Point out each leukocyte.
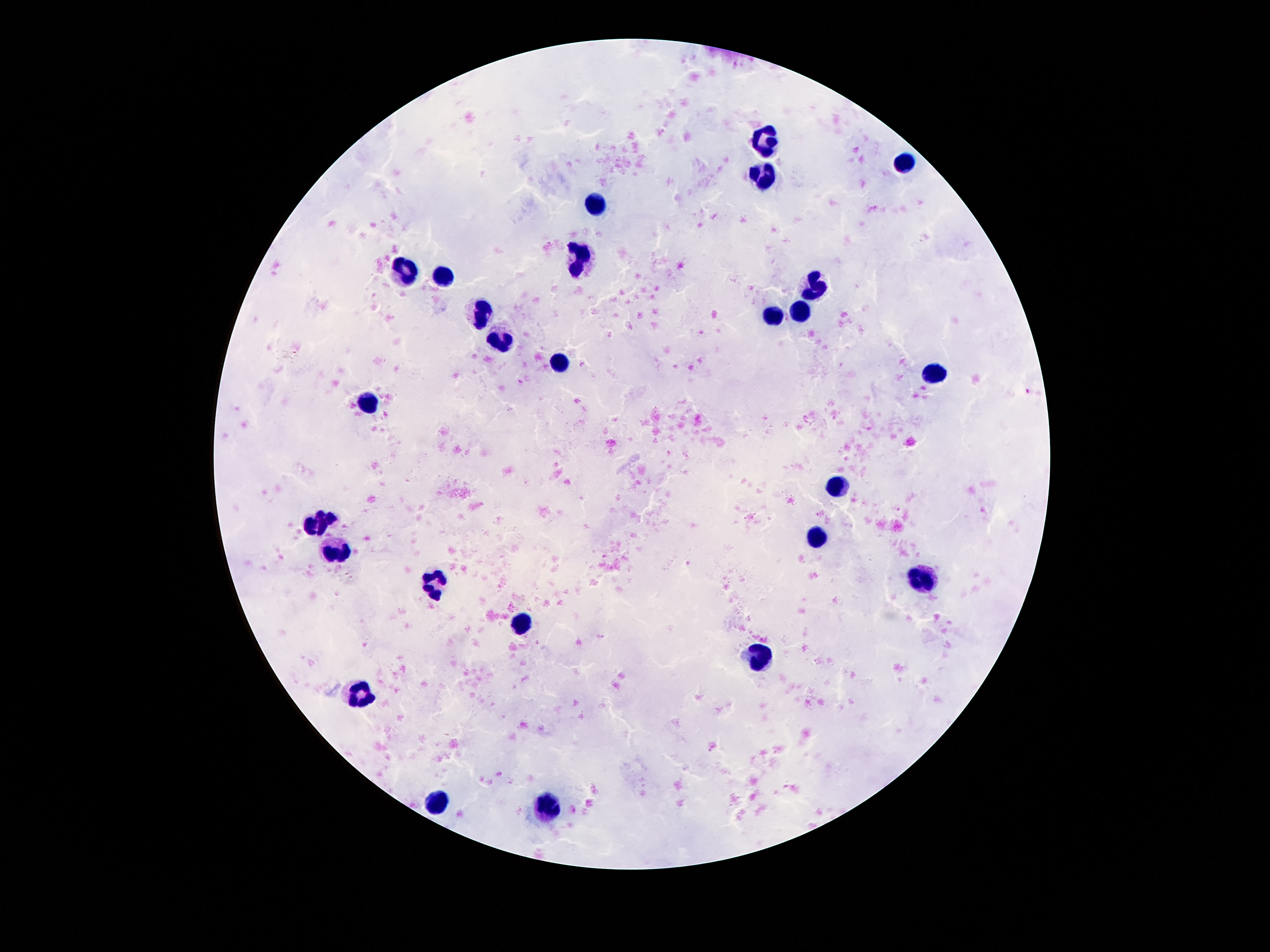
Approximate centers as {x, y} in pixels.
Leukocytes: {763, 142}, {902, 162}, {765, 177}, {593, 206}, {579, 259}, {409, 270}, {443, 275}, {814, 287}, {800, 308}, {484, 313}, {771, 316}, {501, 343}, {562, 365}, {931, 380}, {368, 402}, {839, 484}, {320, 520}, {816, 539}, {339, 559}, {921, 582}, {437, 586}, {519, 623}, {765, 657}, {363, 696}, {437, 801}, {548, 807}.

Summary:
  - Preparation: thick blood film
  - Image size: 1270×952 pixels
  - Stain: Giemsa
  - Magnification: 100x
  - Capture: smartphone camera through the microscope eyepiece
  - Field of view: one from this slide
  - Patient malaria status: not infected